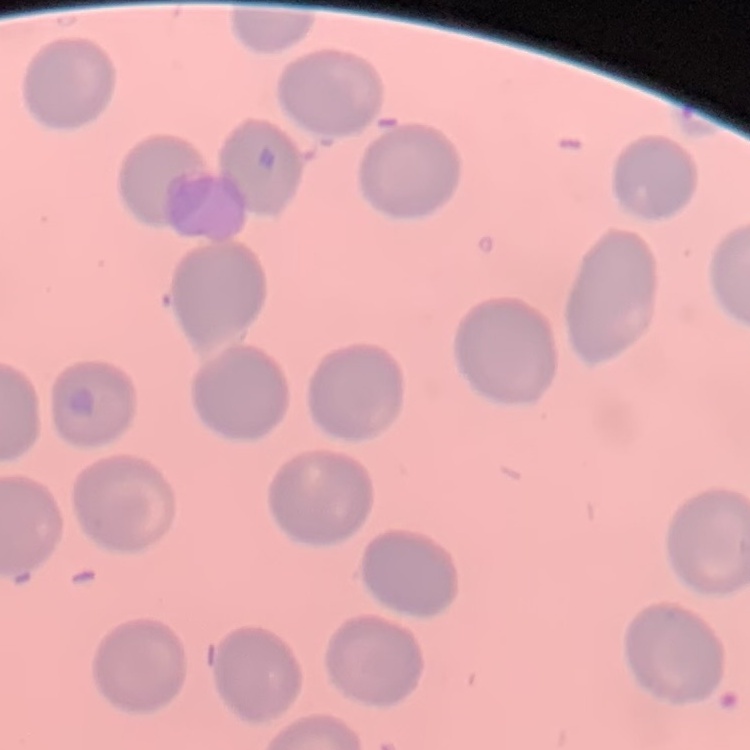

Summary:
  - Erythrocyte morphology: no rouleaux formation
  - Preparation: thin blood smear
  - Stain: Field's or Giemsa
  - Image type: square crop of a larger photomicrograph